Classify this cell by malaria status.
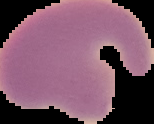

Parasitized.

Summary:
  - Image type: segmented cell region on a black background
  - Image size: 154×124 pixels
  - Preparation: thin blood smear